Identify the parasite.
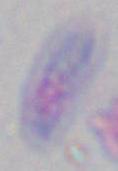
Toxoplasma gondii.

modality = micrograph
magnification = 1000x